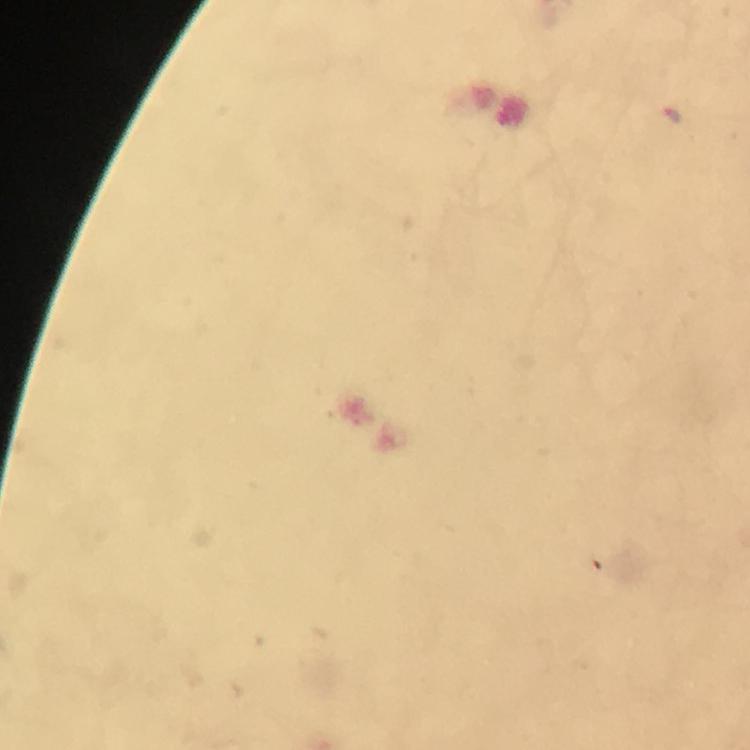

preparation = thick blood smear
context = from a malaria diagnostic workup
immersion oil = applied
image size = 750×750 pixels
capture = smartphone photograph through a microscope
cropped from = a single field of view
magnification = 100x
stain = Giemsa
malaria parasite locations = approximate centers as [x, y] in pixels: [667, 120]